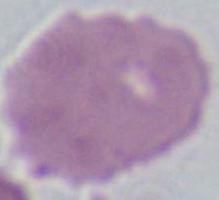 A red blood cell is shown. Micrograph. 1000x magnification.